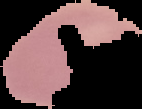

result = negative for malaria parasites
image size = 142×109 pixels
image type = segmented cell region with the area outside set to black
preparation = thin blood film